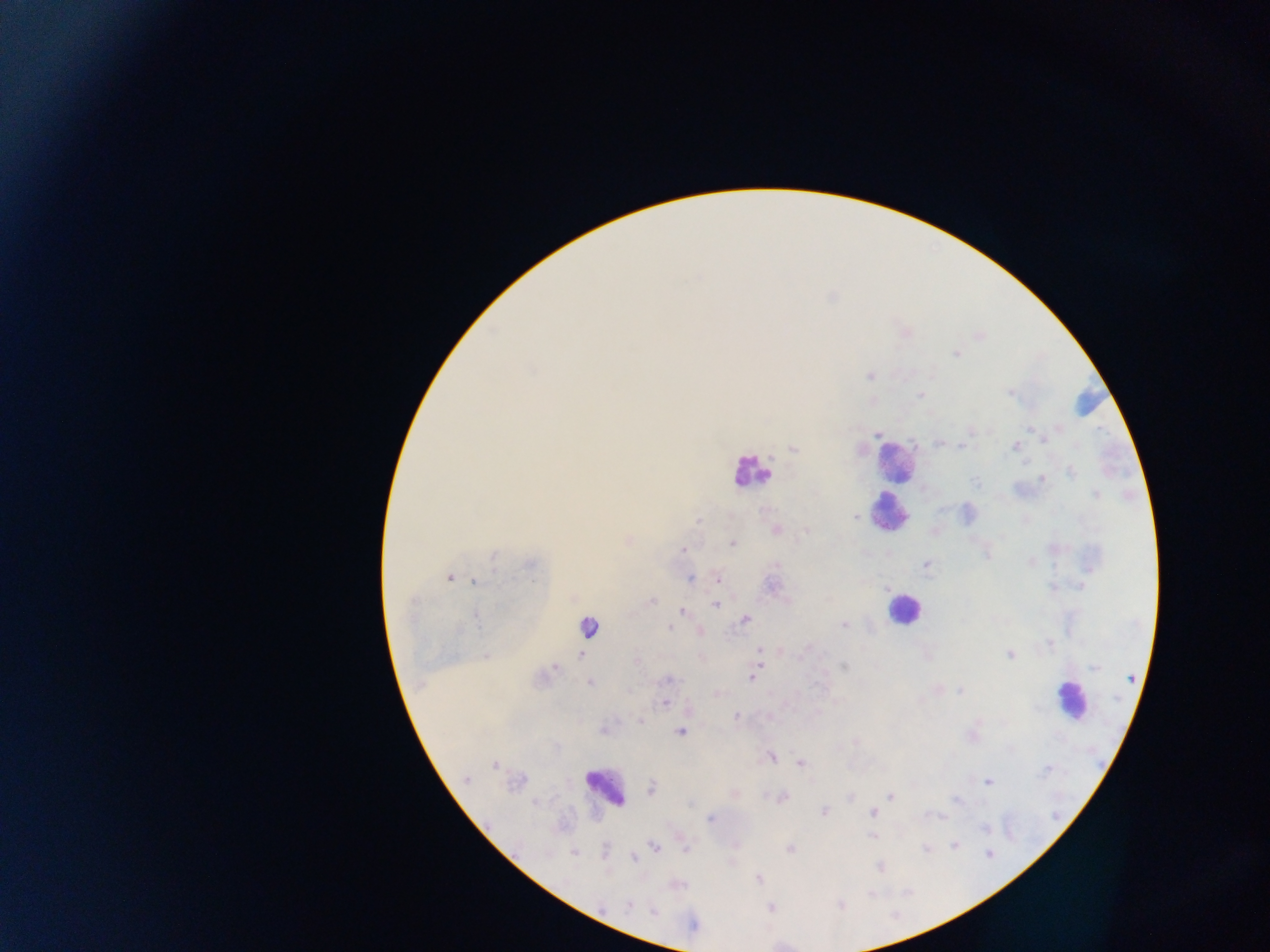

preparation = thick blood film
capture = mobile-phone photograph through a microscope
image size = 1270×952 pixels
Plasmodium parasite locations = approximate centers as [x, y] in pixels: [956, 354], [869, 375], [1010, 394], [920, 395], [1029, 429], [878, 434], [1044, 439], [937, 443], [962, 446], [1016, 446], [792, 448], [1071, 471], [1043, 479], [976, 483], [1096, 494], [855, 517], [698, 520], [775, 530], [807, 531], [628, 541], [733, 544], [684, 549], [987, 555], [494, 556], [1032, 561], [530, 564], [777, 564], [926, 565], [450, 578], [690, 578], [718, 578], [474, 581], [652, 601], [716, 605], [682, 610], [476, 616], [746, 619], [843, 625], [588, 627], [669, 628], [1050, 644], [759, 649], [580, 654], [1010, 654], [636, 662], [555, 667], [844, 667], [1094, 667], [752, 677], [1131, 678], [669, 680], [589, 683], [960, 691], [665, 702], [735, 716], [640, 721], [603, 731], [680, 732], [855, 743], [771, 757], [800, 763], [494, 764], [467, 779], [988, 782], [651, 788], [734, 793], [891, 795], [782, 797], [956, 801], [534, 802], [689, 803], [824, 812], [873, 812], [710, 818], [985, 828], [872, 837], [955, 844], [654, 846], [686, 848], [790, 849], [925, 849], [574, 853], [989, 854], [634, 857], [879, 867], [759, 879], [602, 906], [628, 906], [771, 909], [654, 912]
leukocyte locations = approximate centers as [x, y] in pixels: [894, 460], [750, 472], [890, 512], [903, 609], [1070, 700], [604, 787]
country = Ghana
field of view = single